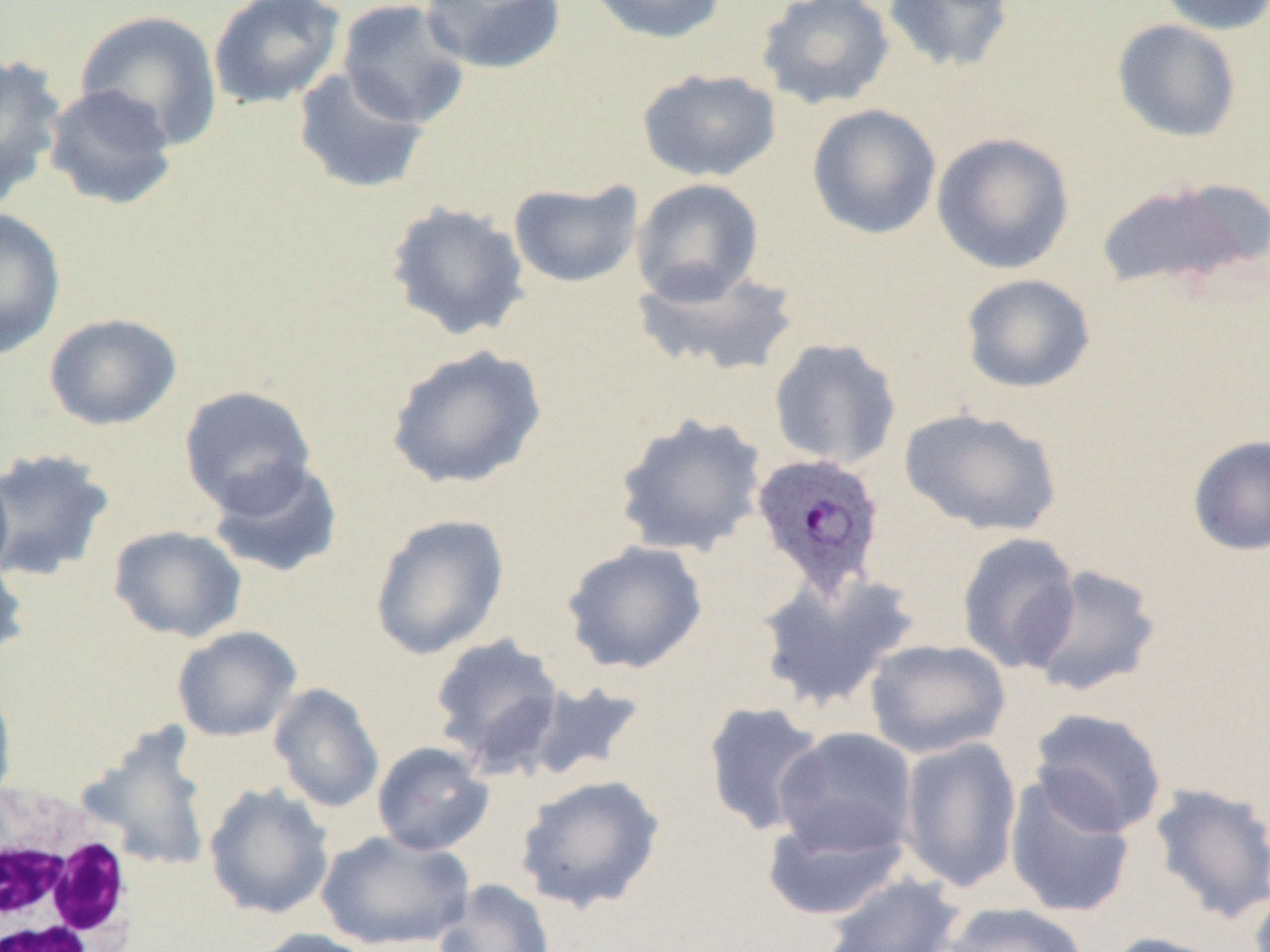

Approximate bounding boxes as named x1/y1/x2/y2 corners in pixels. White blood cell locations: (x1=0, y1=781, x2=143, y2=952). Uninfected red blood cell locations: (x1=207, y1=0, x2=345, y2=110), (x1=336, y1=0, x2=473, y2=129), (x1=420, y1=0, x2=568, y2=75), (x1=584, y1=0, x2=728, y2=44), (x1=755, y1=0, x2=896, y2=111), (x1=882, y1=0, x2=1018, y2=75), (x1=1155, y1=0, x2=1270, y2=35), (x1=74, y1=10, x2=223, y2=150), (x1=1111, y1=19, x2=1242, y2=143), (x1=0, y1=51, x2=67, y2=208), (x1=291, y1=66, x2=431, y2=195), (x1=637, y1=68, x2=782, y2=182), (x1=41, y1=83, x2=179, y2=211), (x1=806, y1=104, x2=942, y2=240), (x1=931, y1=131, x2=1075, y2=274), (x1=630, y1=178, x2=765, y2=305), (x1=1094, y1=178, x2=1263, y2=295), (x1=508, y1=179, x2=644, y2=289), (x1=384, y1=201, x2=531, y2=342), (x1=1, y1=207, x2=66, y2=360), (x1=630, y1=262, x2=800, y2=379), (x1=960, y1=274, x2=1096, y2=394), (x1=44, y1=313, x2=182, y2=431), (x1=768, y1=337, x2=902, y2=470), (x1=385, y1=343, x2=548, y2=490), (x1=178, y1=385, x2=318, y2=515), (x1=899, y1=406, x2=1063, y2=537), (x1=613, y1=412, x2=768, y2=558), (x1=1187, y1=434, x2=1270, y2=556), (x1=0, y1=446, x2=116, y2=583), (x1=206, y1=457, x2=344, y2=579), (x1=0, y1=465, x2=14, y2=589), (x1=369, y1=513, x2=510, y2=660), (x1=108, y1=525, x2=247, y2=643), (x1=957, y1=532, x2=1081, y2=675), (x1=561, y1=540, x2=709, y2=675), (x1=0, y1=554, x2=30, y2=666), (x1=1022, y1=563, x2=1164, y2=698), (x1=755, y1=568, x2=921, y2=713), (x1=172, y1=625, x2=302, y2=743), (x1=428, y1=633, x2=566, y2=774), (x1=864, y1=639, x2=1012, y2=759), (x1=519, y1=679, x2=648, y2=784), (x1=268, y1=682, x2=385, y2=813), (x1=0, y1=684, x2=17, y2=810), (x1=702, y1=700, x2=828, y2=837), (x1=1028, y1=707, x2=1167, y2=837), (x1=78, y1=724, x2=215, y2=874), (x1=774, y1=727, x2=918, y2=859), (x1=899, y1=736, x2=1023, y2=894), (x1=371, y1=741, x2=494, y2=856), (x1=515, y1=773, x2=667, y2=914), (x1=1004, y1=774, x2=1137, y2=918), (x1=203, y1=782, x2=335, y2=920), (x1=1149, y1=782, x2=1270, y2=925), (x1=761, y1=809, x2=909, y2=921), (x1=316, y1=829, x2=475, y2=951), (x1=819, y1=871, x2=966, y2=952), (x1=432, y1=879, x2=554, y2=952), (x1=941, y1=902, x2=1090, y2=952), (x1=247, y1=927, x2=381, y2=952), (x1=1103, y1=932, x2=1231, y2=952). Plasmodium ovale-infected red blood cell locations: (x1=750, y1=452, x2=885, y2=598). Slide-level diagnosis: Plasmodium ovale. Image is 1270×952 pixels. Captured at 1000x magnification. Single field of view. Thin blood smear. Light microscopy.